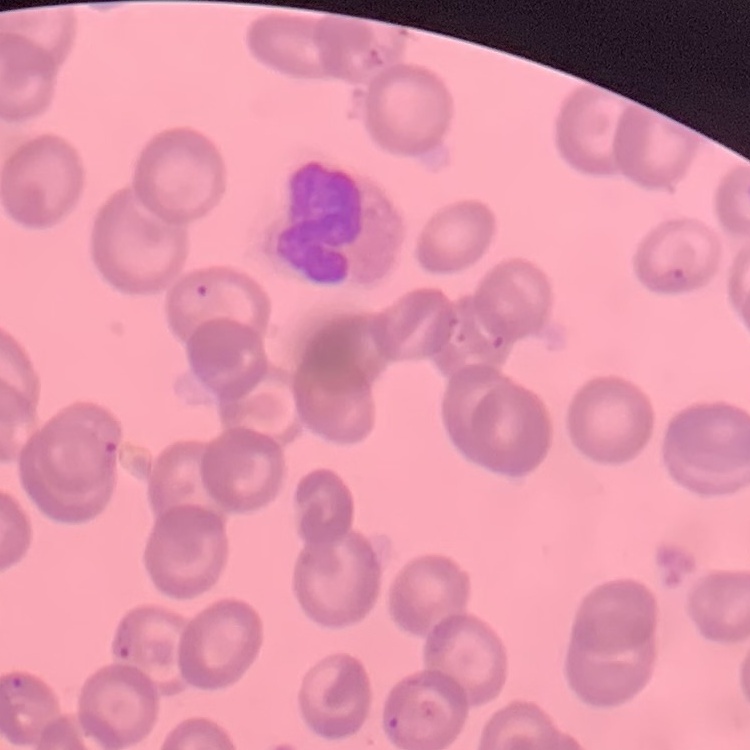
Summary:
  - Erythrocyte morphology: no rouleaux formation
  - Stain: Field's or Giemsa
  - Preparation: thin blood smear
  - Image type: one tile cut from a larger photomicrograph